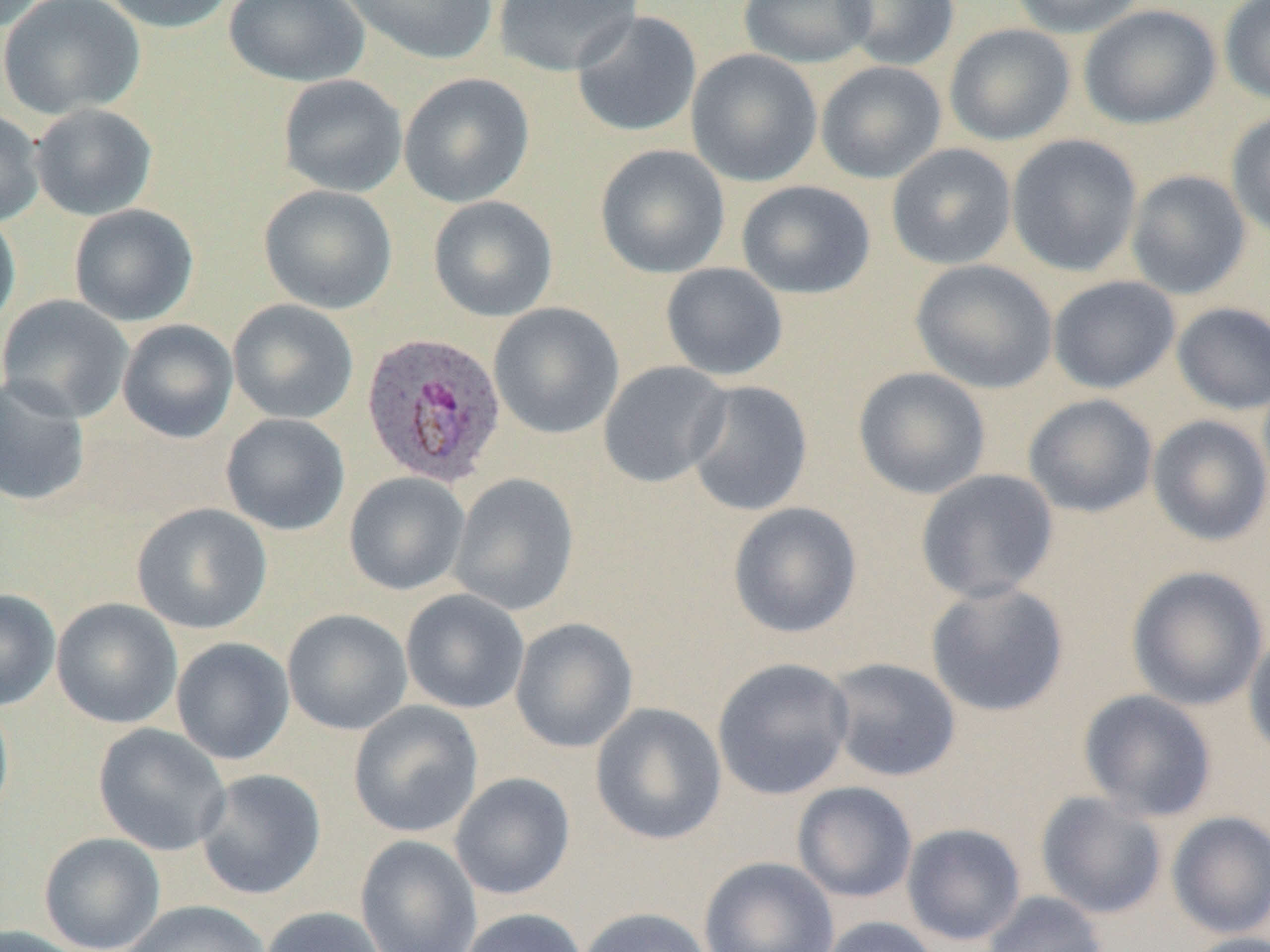
Summary:
  - Coordinate format: approximate bounding boxes as (x1,y1)-(x2,y2) corner pairs in pixels
  - Uninfected red blood cell locations: (0,0)-(146,120), (97,0)-(236,34), (223,0)-(370,87), (339,0)-(499,65), (492,0)-(644,76), (737,0)-(877,68), (835,0)-(960,71), (1009,0)-(1147,38), (1219,0)-(1270,106), (1078,4)-(1221,129), (570,10)-(703,139), (943,23)-(1076,146), (686,48)-(822,187), (815,61)-(947,184), (398,73)-(534,207), (278,74)-(408,197), (29,104)-(158,220), (0,109)-(45,227), (1226,109)-(1270,239), (1006,134)-(1143,277), (595,143)-(730,278), (886,143)-(1017,270), (1125,169)-(1251,299), (736,180)-(876,299), (258,184)-(398,314), (428,195)-(558,321), (68,204)-(199,327), (0,210)-(21,333), (910,259)-(1058,394), (661,263)-(788,381), (1048,275)-(1181,394), (0,295)-(134,422), (227,299)-(359,424), (488,302)-(625,440), (1171,302)-(1270,415), (117,319)-(239,443), (598,361)-(732,488), (853,367)-(991,500), (0,375)-(91,508), (684,380)-(813,517), (1023,394)-(1158,518), (220,413)-(350,535), (1147,414)-(1270,546), (915,468)-(1059,604), (344,472)-(470,595), (449,472)-(579,615), (131,502)-(272,634), (727,502)-(862,639), (1126,565)-(1269,711), (925,581)-(1070,717), (0,588)-(61,711), (400,589)-(530,714), (51,598)-(182,729), (282,609)-(413,735), (510,617)-(639,753), (1244,629)-(1270,762), (171,637)-(295,765), (712,656)-(855,800), (825,657)-(961,782), (1077,688)-(1217,822), (0,695)-(14,825), (348,701)-(484,838), (590,702)-(728,846), (93,723)-(232,856), (195,769)-(326,900), (449,772)-(576,900), (791,781)-(918,903), (1035,791)-(1168,920), (1166,811)-(1270,939), (901,822)-(1026,946), (38,832)-(166,952), (355,834)-(482,952), (699,856)-(839,952), (981,891)-(1109,952), (120,900)-(271,952), (259,906)-(390,952), (575,906)-(715,952), (459,907)-(588,952), (816,916)-(943,952), (0,925)-(89,952), (1183,932)-(1270,952)
  - Plasmodium ovale-infected red blood cell locations: (360,331)-(507,487)
  - Slide-level diagnosis: Plasmodium ovale
  - Preparation: thin blood film
  - Modality: light microscopy
  - Field of view: one of a larger specimen
  - Image size: 1270×952 pixels
  - Magnification: 1000x